Locate every blood parasite and identify its species.
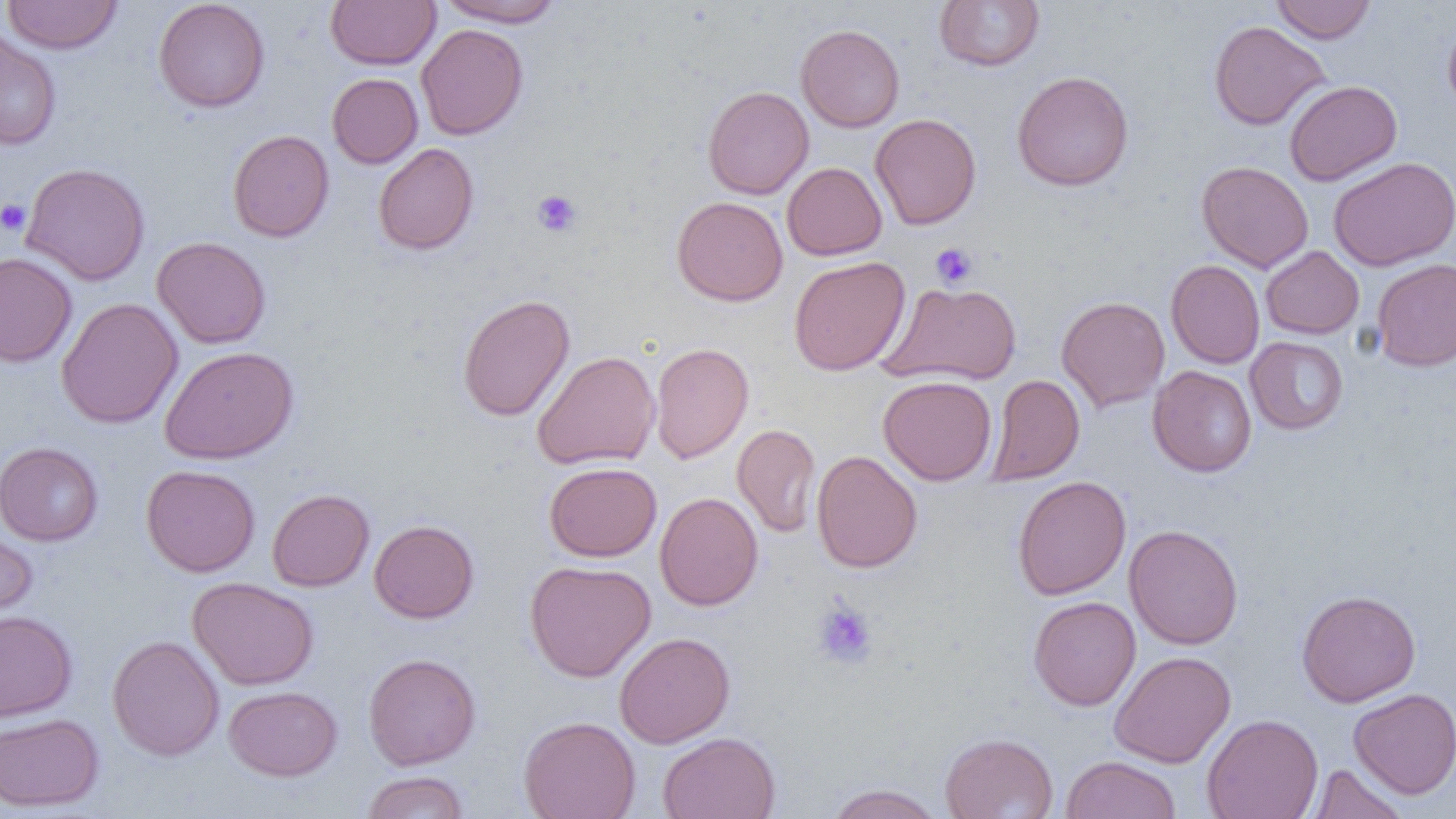
No blood parasites seen.

Approximate bounding boxes as named x1/y1/x2/y2 corners in pixels. Platelet locations: (x1=532, y1=190, x2=582, y2=237), (x1=0, y1=199, x2=31, y2=236), (x1=930, y1=242, x2=978, y2=289), (x1=812, y1=600, x2=878, y2=670). Uninfected red blood cell locations: (x1=1, y1=0, x2=123, y2=54), (x1=153, y1=0, x2=270, y2=112), (x1=325, y1=0, x2=441, y2=70), (x1=435, y1=0, x2=566, y2=27), (x1=934, y1=0, x2=1045, y2=72), (x1=1271, y1=0, x2=1377, y2=44), (x1=1443, y1=17, x2=1456, y2=118), (x1=1208, y1=20, x2=1331, y2=130), (x1=416, y1=23, x2=528, y2=140), (x1=795, y1=24, x2=905, y2=132), (x1=0, y1=28, x2=61, y2=150), (x1=1011, y1=70, x2=1134, y2=191), (x1=327, y1=73, x2=423, y2=169), (x1=1284, y1=80, x2=1402, y2=185), (x1=703, y1=85, x2=814, y2=199), (x1=870, y1=113, x2=982, y2=230), (x1=228, y1=129, x2=335, y2=242), (x1=373, y1=143, x2=479, y2=255), (x1=1328, y1=156, x2=1456, y2=271), (x1=1196, y1=161, x2=1314, y2=273), (x1=20, y1=162, x2=150, y2=286), (x1=782, y1=162, x2=887, y2=261), (x1=671, y1=196, x2=788, y2=306), (x1=152, y1=236, x2=271, y2=349), (x1=1261, y1=246, x2=1364, y2=339), (x1=0, y1=252, x2=77, y2=368), (x1=789, y1=256, x2=911, y2=376), (x1=1371, y1=258, x2=1456, y2=371), (x1=1166, y1=259, x2=1265, y2=369), (x1=880, y1=281, x2=1022, y2=386), (x1=458, y1=294, x2=575, y2=422), (x1=1056, y1=296, x2=1170, y2=412), (x1=56, y1=297, x2=184, y2=429), (x1=1244, y1=336, x2=1349, y2=435), (x1=649, y1=342, x2=754, y2=463), (x1=160, y1=345, x2=299, y2=464), (x1=532, y1=350, x2=660, y2=470), (x1=1148, y1=365, x2=1257, y2=477), (x1=985, y1=374, x2=1085, y2=486), (x1=878, y1=375, x2=997, y2=485), (x1=732, y1=424, x2=820, y2=537), (x1=0, y1=441, x2=103, y2=546), (x1=811, y1=450, x2=922, y2=573), (x1=544, y1=461, x2=662, y2=562), (x1=140, y1=464, x2=260, y2=577), (x1=1012, y1=475, x2=1131, y2=600), (x1=267, y1=488, x2=374, y2=591), (x1=654, y1=492, x2=763, y2=611), (x1=368, y1=519, x2=479, y2=623), (x1=1124, y1=524, x2=1243, y2=650), (x1=0, y1=525, x2=37, y2=628), (x1=524, y1=559, x2=656, y2=682), (x1=187, y1=576, x2=319, y2=690), (x1=1296, y1=589, x2=1421, y2=707), (x1=1028, y1=595, x2=1141, y2=711), (x1=0, y1=610, x2=77, y2=721), (x1=614, y1=631, x2=735, y2=748), (x1=107, y1=635, x2=225, y2=761), (x1=1108, y1=650, x2=1237, y2=768), (x1=363, y1=652, x2=481, y2=770), (x1=223, y1=685, x2=342, y2=781), (x1=1348, y1=687, x2=1456, y2=799), (x1=0, y1=713, x2=104, y2=812), (x1=1202, y1=713, x2=1324, y2=819), (x1=518, y1=715, x2=641, y2=819), (x1=658, y1=732, x2=780, y2=819), (x1=940, y1=732, x2=1058, y2=819), (x1=1061, y1=755, x2=1181, y2=819), (x1=1307, y1=764, x2=1408, y2=819), (x1=361, y1=771, x2=470, y2=818), (x1=823, y1=783, x2=946, y2=819). Slide-level diagnosis: no evidence of blood parasites. Light microscopy. Thin blood smear. Captured at 1000x magnification. Image is 1456×819 pixels. One field of a larger specimen.